Locate every malaria parasite.
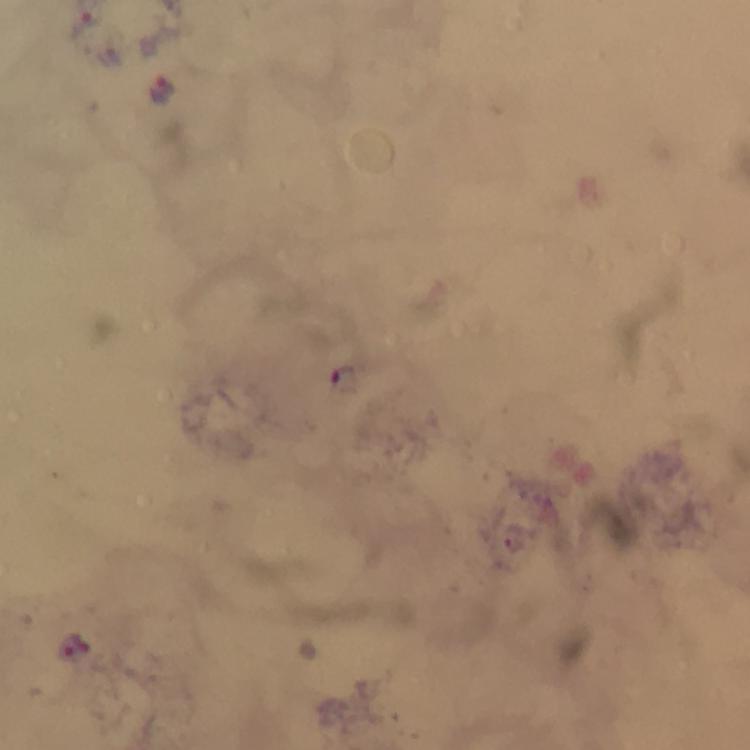

Approximate object centers, in pixels from the top-left corner.
Malaria parasites: (x=86, y=18), (x=161, y=91), (x=77, y=644).

context = from a malaria diagnostic workup
capture = smartphone photograph through a microscope
cropped from = a single field of view
image size = 750×750 pixels
stain = Giemsa
preparation = thick blood smear
magnification = 100x
immersion oil = applied